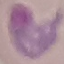

Result: malaria parasites detected. Thin blood film. Automatically extracted cell patch, resized to 64 × 64 pixels. Acquired by smartphone through the microscope eyepiece. Giemsa-stained preparation.